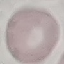
result: negative for malaria parasites
preparation: thin blood smear
stain: Giemsa
image_type: automatically extracted cell patch, resized to 64 × 64 pixels
capture: smartphone camera at the microscope eyepiece